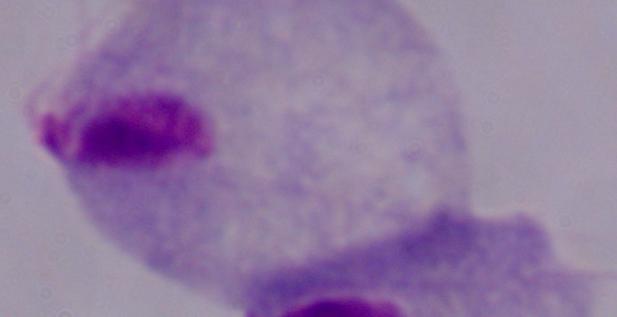

Summary:
  - Identification: trichomonad
  - Modality: photomicrograph
  - Magnification: 1000x